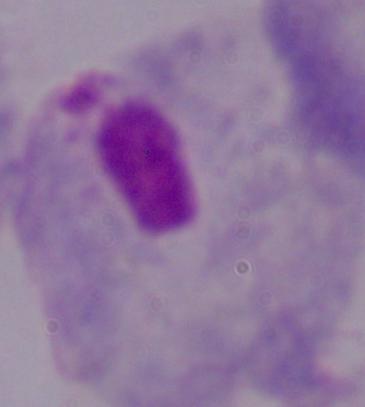
identification = trichomonad
magnification = 1000x
modality = micrograph